Report the malaria status of this cell.
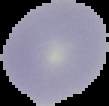

It is uninfected.

{
  "image_size": "109×106 pixels",
  "preparation": "thin blood film",
  "image_type": "cell region segmented out of the field of view; surrounding area masked to black"
}